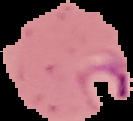
result = Plasmodium parasites detected
preparation = thin blood smear
image type = cell region segmented out of the field of view; surrounding area masked to black
image size = 133×121 pixels